Assess this cell for malaria.
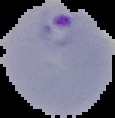

Parasitized.

Image is 115×118 pixels. Segmented cell region on a black background. From a thin blood film.